Assess for malaria.
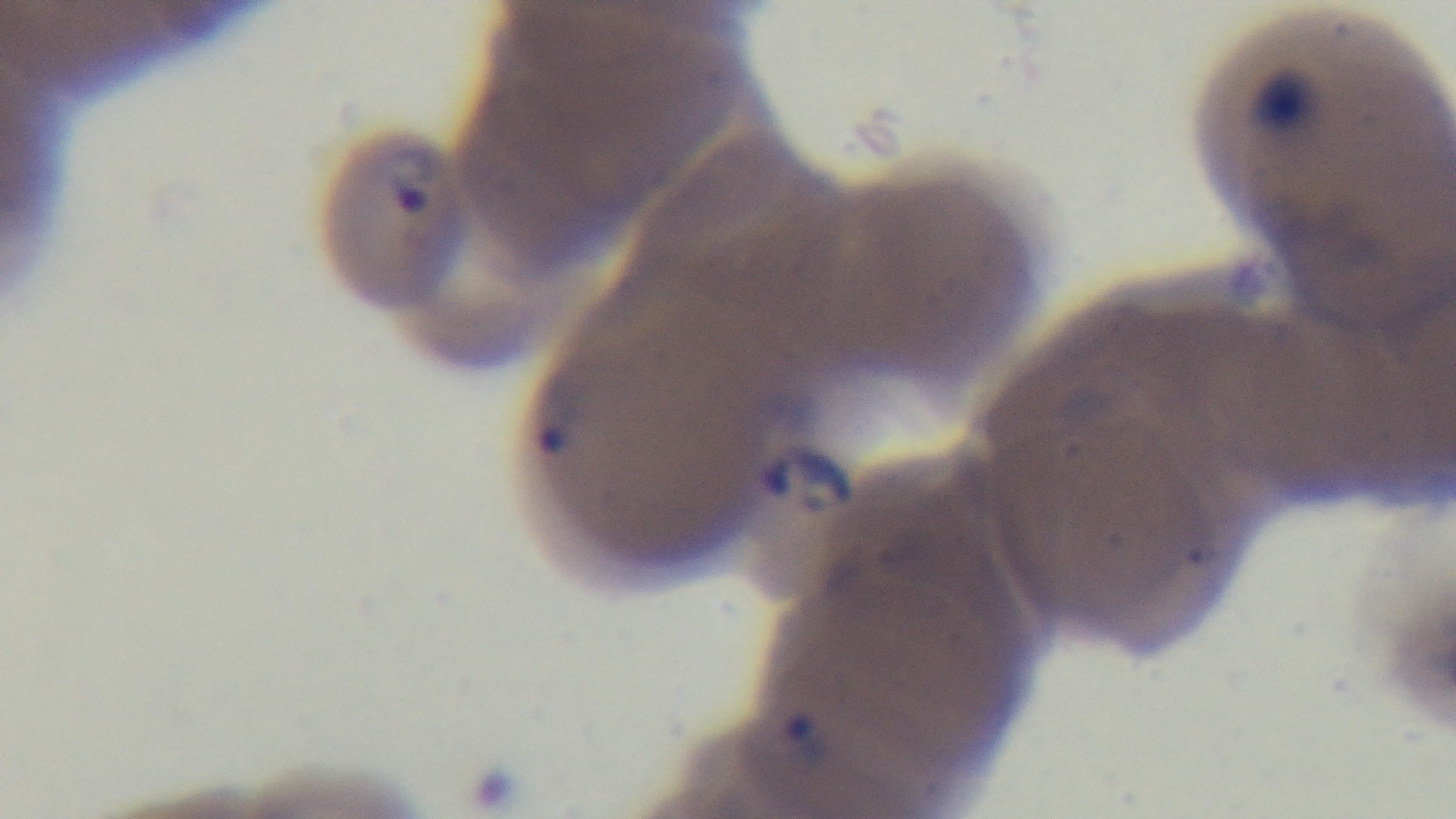

It is infected.

Mounted 4K digital camera. Giemsa-stained. Single field of view. Light microscopy. Preparation: thin blood film. 100x oil-immersion objective.